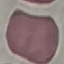
Summary:
  - Result: negative for malaria parasites
  - Image type: cell patch, automatically extracted from a larger field of view and resized to 64 × 64 pixels
  - Preparation: thin blood smear
  - Stain: Giemsa
  - Capture: smartphone through the microscope eyepiece